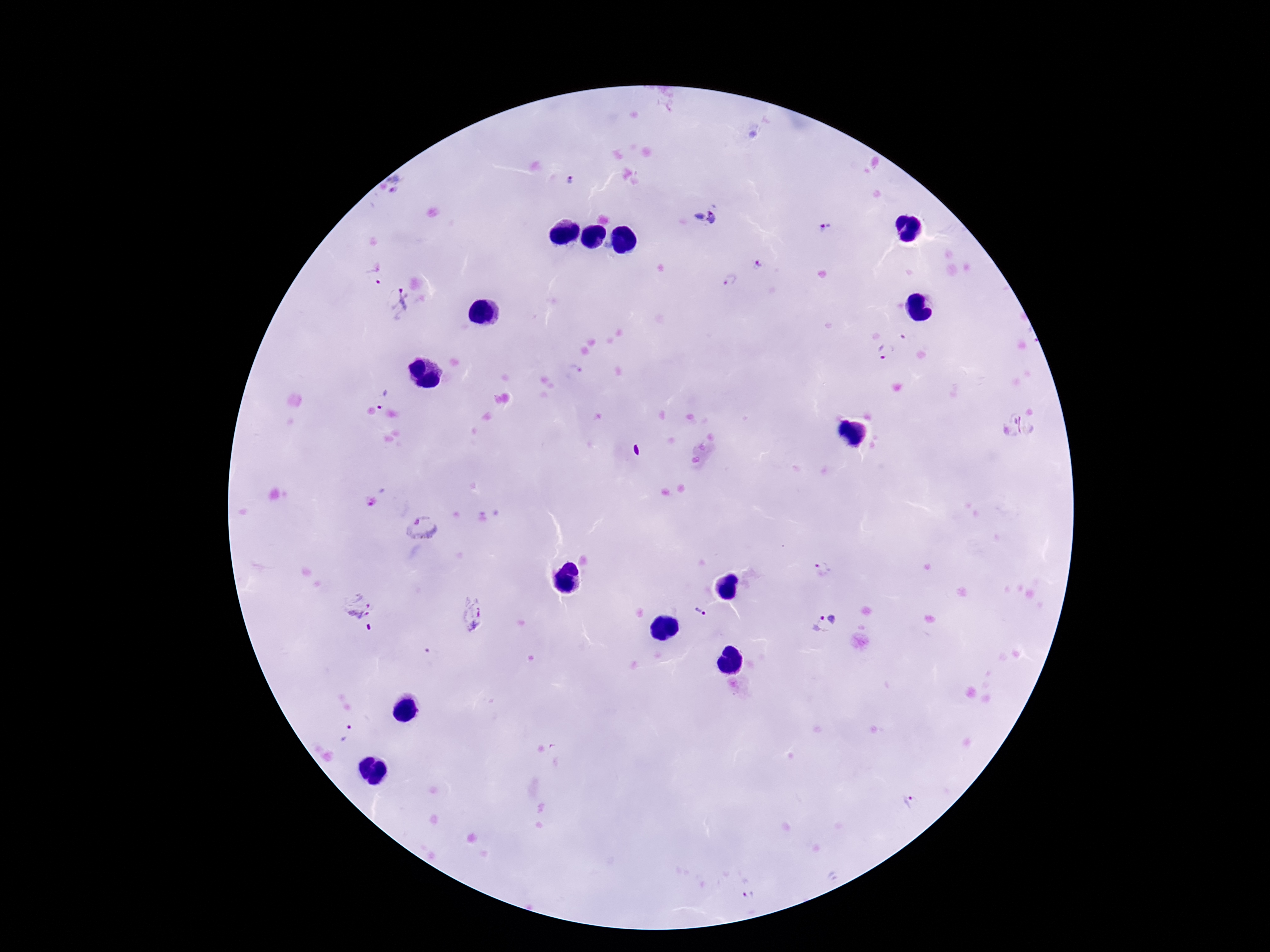
{
  "stain": "Giemsa",
  "capture": "smartphone camera through the microscope eyepiece",
  "field_of_view": "single",
  "magnification": "100x",
  "image_size": "1270×952 pixels",
  "preparation": "thick blood smear",
  "patient_malaria_status": "positive",
  "plasmodium_parasite_locations": "approximate centers as {x, y} in pixels: {570, 181}, {400, 184}, {705, 220}, {823, 228}, {759, 266}, {375, 273}, {730, 280}, {401, 303}, {910, 338}, {886, 352}, {575, 373}, {381, 398}, {1022, 424}, {421, 525}, {823, 568}, {357, 603}, {701, 612}, {472, 614}, {826, 623}, {348, 734}, {912, 801}, {748, 895}"
}